Report the malaria status of this cell.
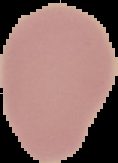

It is uninfected.

image_type: cell region segmented out of the field of view; surrounding area masked to black
preparation: thin blood film
image_size: 118×163 pixels